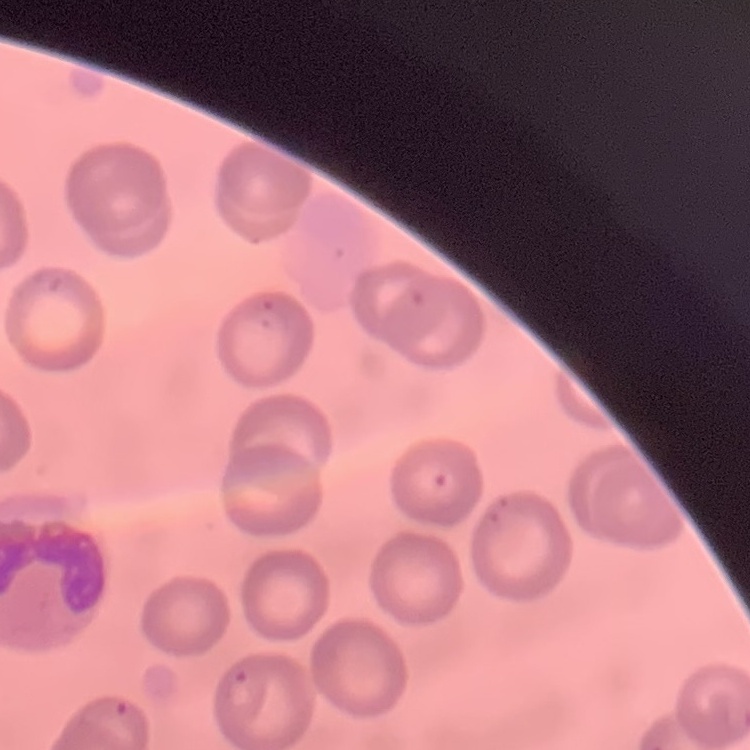
Summary:
  - Erythrocyte morphology: no rouleaux formation
  - Preparation: thin blood film
  - Image type: one tile cut from a larger photomicrograph
  - Stain: Field's or Giemsa